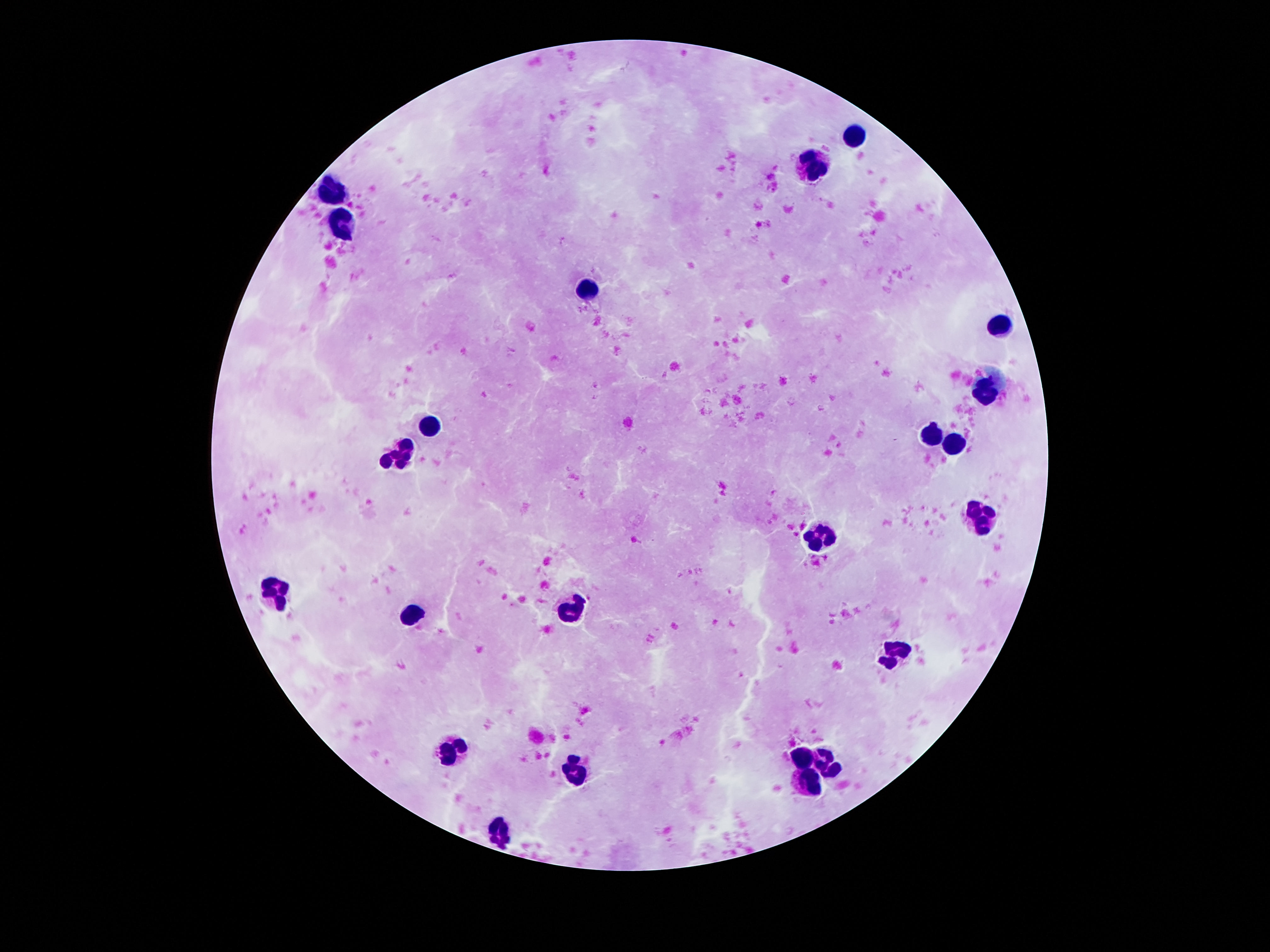
Approximate centers as (x, y) in pixels.
Summary:
  - Leukocyte locations: (853, 135), (815, 164), (333, 193), (345, 226), (587, 290), (999, 326), (987, 395), (431, 423), (931, 436), (955, 446), (401, 452), (985, 517), (823, 540), (279, 589), (575, 608), (417, 613), (891, 655), (451, 750), (805, 755), (829, 763), (577, 774), (811, 782), (499, 834)
  - Capture: smartphone camera through the microscope eyepiece
  - Preparation: thick blood film
  - Magnification: 100x
  - Patient malaria status: negative
  - Stain: Giemsa
  - Image size: 1270×952 pixels
  - Field of view: single